Identify the parasite.
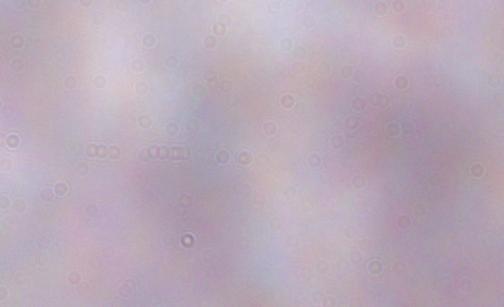
This is a trypanosome.

1000x magnification. Micrograph.